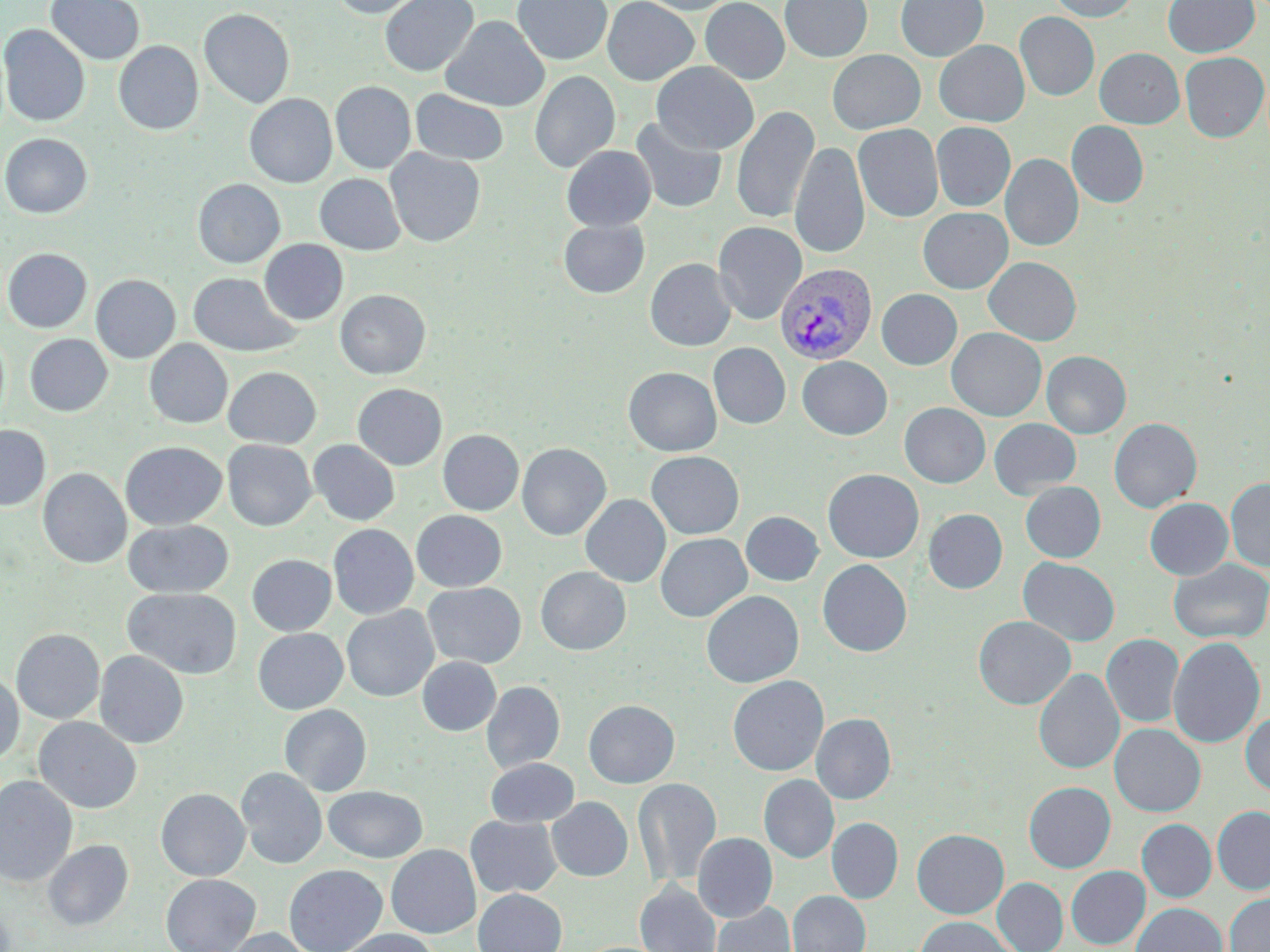

{
  "plasmodium_vivax_infected_red_blood_cell_locations": "approximate bounding boxes as named x1/y1/x2/y2 corners in pixels: (x1=774, y1=263, x2=878, y2=365)",
  "slide_level_diagnosis": "Plasmodium vivax",
  "stain": "May-Grünwald-Giemsa",
  "magnification": "1000x",
  "modality": "light microscopy",
  "uninfected_red_blood_cell_locations": "approximate bounding boxes as named x1/y1/x2/y2 corners in pixels: (x1=45, y1=0, x2=145, y2=65), (x1=329, y1=0, x2=424, y2=18), (x1=379, y1=0, x2=478, y2=77), (x1=513, y1=0, x2=612, y2=65), (x1=602, y1=0, x2=699, y2=85), (x1=636, y1=0, x2=738, y2=15), (x1=700, y1=0, x2=789, y2=84), (x1=780, y1=0, x2=873, y2=62), (x1=895, y1=0, x2=988, y2=61), (x1=1047, y1=0, x2=1140, y2=22), (x1=1162, y1=0, x2=1259, y2=58), (x1=198, y1=8, x2=295, y2=109), (x1=1015, y1=12, x2=1099, y2=101), (x1=441, y1=16, x2=549, y2=112), (x1=0, y1=24, x2=90, y2=126), (x1=934, y1=40, x2=1029, y2=127), (x1=114, y1=41, x2=203, y2=135), (x1=1094, y1=48, x2=1184, y2=128), (x1=827, y1=49, x2=925, y2=134), (x1=1179, y1=52, x2=1268, y2=142), (x1=652, y1=62, x2=758, y2=155), (x1=529, y1=70, x2=620, y2=173), (x1=330, y1=81, x2=416, y2=174), (x1=410, y1=89, x2=509, y2=166), (x1=244, y1=93, x2=337, y2=188), (x1=731, y1=105, x2=820, y2=224), (x1=630, y1=116, x2=727, y2=214), (x1=931, y1=121, x2=1016, y2=212), (x1=1067, y1=121, x2=1149, y2=207), (x1=853, y1=124, x2=943, y2=223), (x1=0, y1=133, x2=93, y2=218), (x1=790, y1=141, x2=869, y2=260), (x1=561, y1=145, x2=657, y2=231), (x1=385, y1=148, x2=486, y2=247), (x1=1001, y1=154, x2=1083, y2=251), (x1=314, y1=173, x2=406, y2=255), (x1=193, y1=179, x2=285, y2=268), (x1=918, y1=207, x2=1013, y2=294), (x1=558, y1=220, x2=649, y2=298), (x1=712, y1=221, x2=807, y2=325), (x1=259, y1=239, x2=348, y2=325), (x1=2, y1=248, x2=92, y2=333), (x1=983, y1=257, x2=1081, y2=345), (x1=645, y1=258, x2=736, y2=352), (x1=188, y1=272, x2=301, y2=356), (x1=91, y1=274, x2=180, y2=363), (x1=335, y1=289, x2=430, y2=379), (x1=876, y1=289, x2=962, y2=370), (x1=947, y1=327, x2=1046, y2=421), (x1=25, y1=334, x2=112, y2=416), (x1=144, y1=339, x2=233, y2=428), (x1=708, y1=343, x2=791, y2=429), (x1=144, y1=350, x2=322, y2=436), (x1=1042, y1=351, x2=1131, y2=438), (x1=797, y1=356, x2=892, y2=439), (x1=223, y1=366, x2=321, y2=448), (x1=623, y1=367, x2=722, y2=456), (x1=352, y1=383, x2=447, y2=471), (x1=899, y1=403, x2=990, y2=488), (x1=899, y1=412, x2=1084, y2=491), (x1=989, y1=418, x2=1081, y2=498), (x1=1109, y1=418, x2=1202, y2=513), (x1=0, y1=424, x2=51, y2=511), (x1=438, y1=430, x2=524, y2=516), (x1=309, y1=439, x2=400, y2=525), (x1=222, y1=440, x2=316, y2=531), (x1=120, y1=441, x2=226, y2=530), (x1=517, y1=443, x2=611, y2=540), (x1=646, y1=451, x2=743, y2=539), (x1=38, y1=468, x2=132, y2=568), (x1=822, y1=469, x2=924, y2=562), (x1=1226, y1=478, x2=1270, y2=572), (x1=1020, y1=482, x2=1105, y2=562), (x1=581, y1=494, x2=670, y2=587), (x1=1145, y1=497, x2=1233, y2=580), (x1=923, y1=509, x2=1008, y2=593), (x1=411, y1=510, x2=507, y2=592), (x1=741, y1=511, x2=824, y2=586), (x1=123, y1=519, x2=233, y2=598), (x1=328, y1=524, x2=418, y2=620), (x1=655, y1=533, x2=752, y2=622), (x1=247, y1=554, x2=336, y2=636), (x1=1018, y1=557, x2=1120, y2=647), (x1=817, y1=559, x2=912, y2=657), (x1=1168, y1=559, x2=1270, y2=644), (x1=535, y1=566, x2=631, y2=655), (x1=423, y1=582, x2=526, y2=668), (x1=123, y1=588, x2=241, y2=679), (x1=701, y1=591, x2=804, y2=688), (x1=342, y1=605, x2=439, y2=702), (x1=974, y1=616, x2=1075, y2=709), (x1=253, y1=628, x2=348, y2=714), (x1=11, y1=629, x2=105, y2=724), (x1=1101, y1=633, x2=1184, y2=727), (x1=1168, y1=636, x2=1266, y2=749), (x1=94, y1=650, x2=189, y2=748), (x1=417, y1=657, x2=501, y2=736), (x1=1034, y1=669, x2=1124, y2=774), (x1=0, y1=673, x2=24, y2=765), (x1=727, y1=675, x2=829, y2=776), (x1=481, y1=681, x2=565, y2=773), (x1=583, y1=699, x2=679, y2=788), (x1=279, y1=704, x2=372, y2=796), (x1=1240, y1=711, x2=1270, y2=797), (x1=812, y1=713, x2=896, y2=804), (x1=34, y1=717, x2=142, y2=814), (x1=1109, y1=724, x2=1205, y2=816), (x1=485, y1=758, x2=579, y2=827), (x1=235, y1=768, x2=327, y2=869), (x1=0, y1=774, x2=78, y2=887), (x1=758, y1=775, x2=839, y2=863), (x1=633, y1=777, x2=722, y2=889), (x1=1024, y1=782, x2=1115, y2=872), (x1=323, y1=786, x2=427, y2=862), (x1=155, y1=788, x2=250, y2=881), (x1=547, y1=796, x2=633, y2=881), (x1=1212, y1=806, x2=1270, y2=894), (x1=465, y1=815, x2=562, y2=898), (x1=827, y1=817, x2=903, y2=903), (x1=1137, y1=819, x2=1216, y2=902), (x1=912, y1=829, x2=1009, y2=918), (x1=693, y1=832, x2=777, y2=922), (x1=42, y1=839, x2=133, y2=931), (x1=386, y1=844, x2=481, y2=938), (x1=283, y1=864, x2=388, y2=952), (x1=1066, y1=866, x2=1150, y2=949), (x1=161, y1=874, x2=261, y2=952), (x1=993, y1=878, x2=1068, y2=952), (x1=635, y1=881, x2=721, y2=952), (x1=473, y1=889, x2=567, y2=952), (x1=787, y1=890, x2=870, y2=952), (x1=1224, y1=892, x2=1270, y2=952), (x1=711, y1=902, x2=796, y2=952), (x1=1130, y1=902, x2=1227, y2=952), (x1=915, y1=916, x2=1018, y2=952), (x1=222, y1=927, x2=316, y2=952), (x1=336, y1=928, x2=441, y2=952)",
  "preparation": "thin blood smear",
  "field_of_view": "one of a larger specimen",
  "image_size": "1270×952 pixels"
}